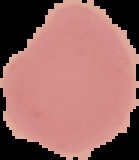

Summary:
  - Preparation: thin blood film
  - Image type: segmented cell region on a black background
  - Image size: 139×160 pixels
  - Result: negative for Plasmodium parasites